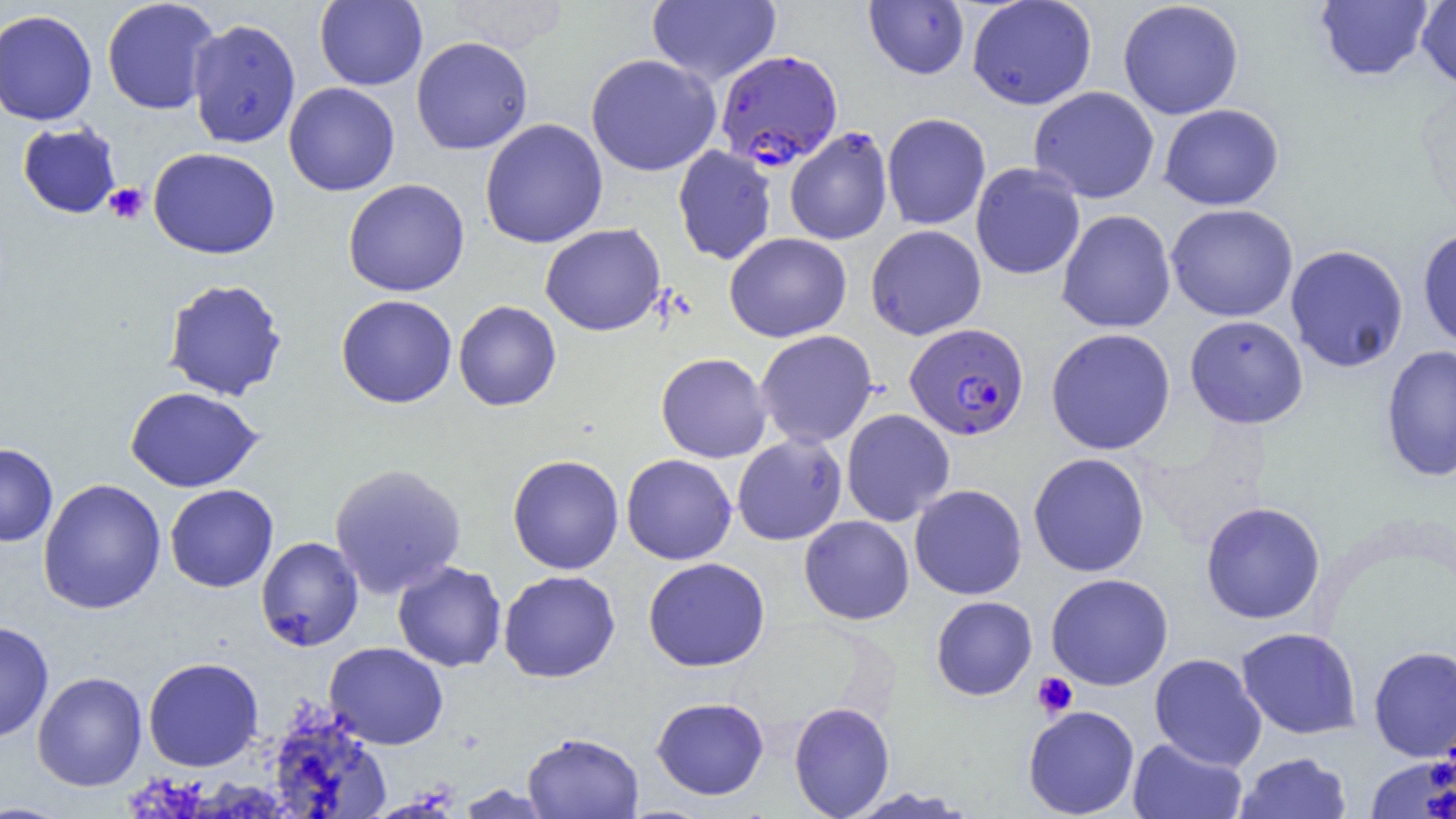
slide-level diagnosis = Plasmodium falciparum
field of view = one of a larger specimen
Plasmodium falciparum-infected red blood cell locations = approximate bounding boxes as (x1, y1, x2, y2) in pixels: (714, 49, 843, 170), (904, 323, 1029, 441)
uninfected red blood cell locations = approximate bounding boxes as (x1, y1, x2, y2) in pixels: (102, 0, 220, 115), (314, 0, 428, 90), (646, 0, 781, 86), (967, 0, 1097, 110), (1117, 0, 1244, 119), (864, 1, 970, 79), (1314, 1, 1434, 82), (1417, 1, 1456, 91), (0, 9, 98, 126), (187, 18, 301, 148), (411, 36, 533, 155), (585, 53, 721, 177), (283, 82, 400, 196), (1029, 86, 1160, 204), (1158, 104, 1284, 211), (882, 113, 991, 230), (479, 118, 608, 249), (17, 122, 122, 219), (784, 127, 893, 245), (672, 145, 777, 265), (148, 147, 280, 259), (970, 162, 1086, 280), (343, 178, 470, 296), (1166, 203, 1298, 322), (1057, 209, 1176, 333), (540, 223, 666, 336), (866, 224, 986, 340), (1417, 226, 1456, 350), (724, 232, 852, 342), (1285, 244, 1409, 373), (161, 278, 288, 402), (335, 294, 457, 408), (453, 300, 562, 411), (1184, 315, 1309, 429), (1046, 328, 1176, 455), (755, 330, 878, 448), (1380, 344, 1456, 483), (656, 352, 772, 463), (124, 386, 264, 492), (841, 408, 955, 526), (732, 434, 847, 545), (0, 442, 58, 547), (1028, 452, 1150, 577), (507, 454, 624, 574), (621, 454, 737, 565), (329, 463, 467, 599), (38, 478, 166, 614), (164, 484, 279, 592), (909, 484, 1027, 600), (1200, 501, 1326, 624), (799, 515, 914, 625), (255, 536, 364, 651), (643, 557, 770, 672), (392, 560, 507, 672), (498, 570, 621, 682), (1045, 573, 1174, 690), (930, 595, 1038, 700), (0, 620, 54, 744), (1236, 627, 1362, 739), (324, 642, 449, 750), (1368, 645, 1456, 761), (1150, 653, 1267, 770), (143, 656, 264, 771), (32, 671, 147, 791), (651, 696, 769, 800), (789, 701, 894, 818), (1023, 705, 1140, 818), (268, 713, 392, 819), (522, 731, 644, 818), (1127, 737, 1247, 819), (1235, 751, 1351, 819), (1366, 754, 1456, 819), (455, 783, 556, 818), (842, 786, 977, 818), (0, 802, 74, 818)
modality = light microscopy
platelet locations = approximate bounding boxes as (x1, y1, x2, y2) in pixels: (104, 183, 148, 224), (1032, 672, 1078, 718)
image size = 1456×819 pixels
magnification = 1000x
preparation = thin blood film